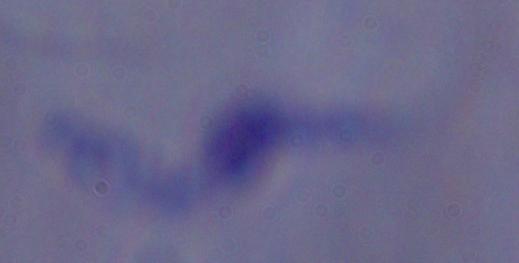

Summary:
  - Magnification: 1000x
  - Identification: trypanosome
  - Modality: photomicrograph